Assess the morphology of the red blood cells.
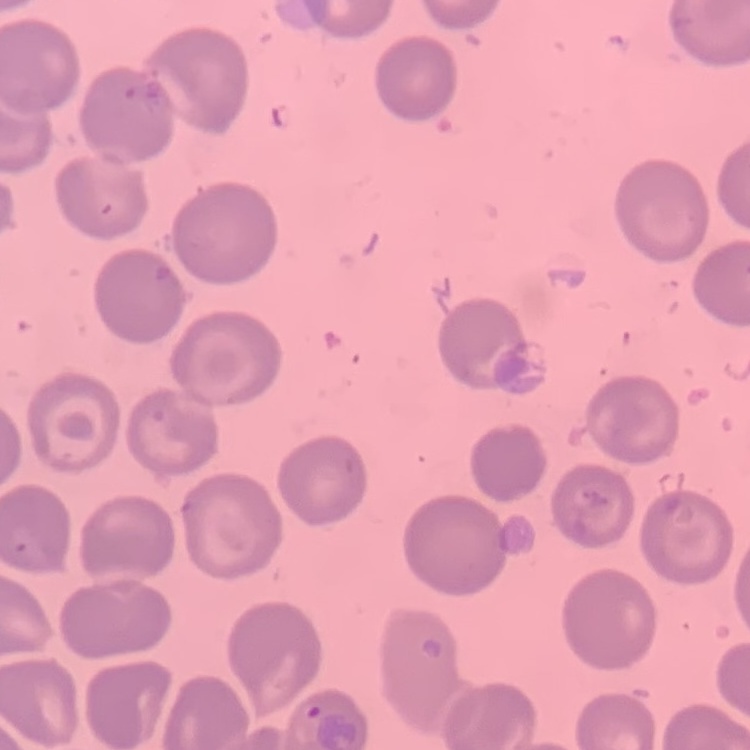
No rouleaux formation.

Summary:
  - Image type: one tile cut from a larger photomicrograph
  - Stain: Field's or Giemsa
  - Preparation: thin blood smear